Comment on the morphology of the red blood cells.
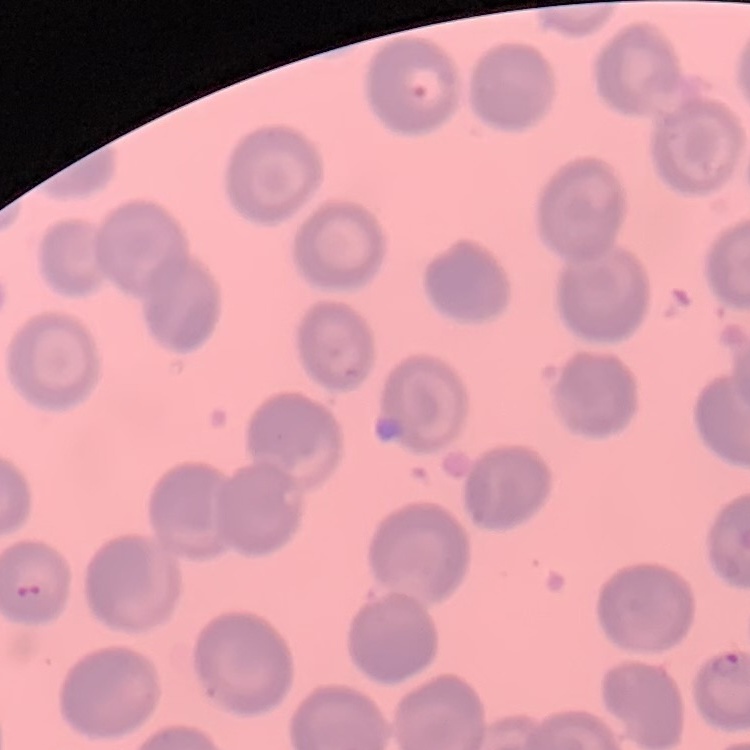
They show no rouleaux formation.

image type = one tile cut from a larger photomicrograph
preparation = thin peripheral smear
stain = Field's or Giemsa